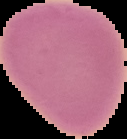 Image is 127×139 pixels. Result: no Plasmodium parasites detected. From a thin blood film. Cell region segmented out of the field of view; the surrounding area is masked to black.